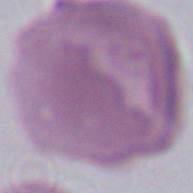
Photomicrograph. 1000x magnification. An erythrocyte is seen.